Report the malaria status of this cell.
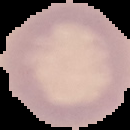

Uninfected.

Summary:
  - Image size: 130×130 pixels
  - Preparation: thin blood smear
  - Image type: segmented cell region on a black background